Classify this cell by malaria status.
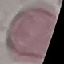
Uninfected.

Thin blood film. Giemsa-stained preparation. Cell patch, automatically extracted from a larger field of view and resized to 64 × 64 pixels. Photographed with a smartphone camera at the microscope eyepiece.